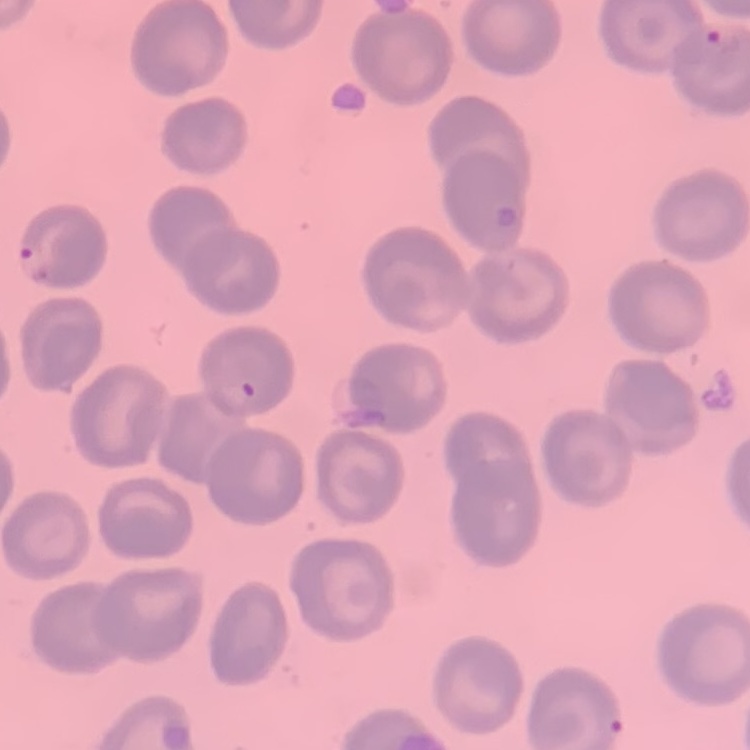

red_blood_cell_morphology: no rouleaux formation
preparation: thin peripheral smear
image_type: one tile cut from a larger photomicrograph
stain: Field's or Giemsa